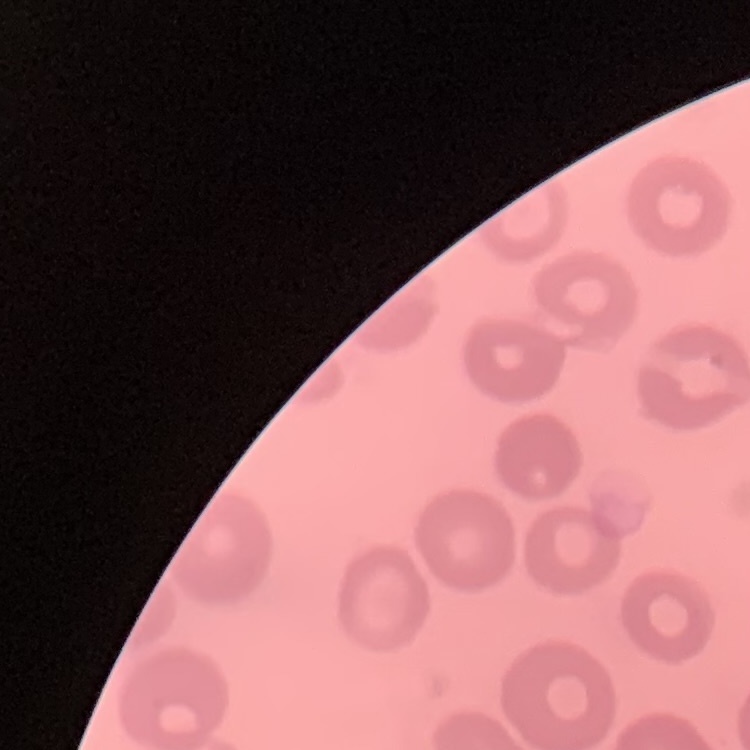
red_blood_cell_morphology: no rouleaux formation
stain: Field's or Giemsa
preparation: thin peripheral smear
image_type: square crop of a larger photomicrograph